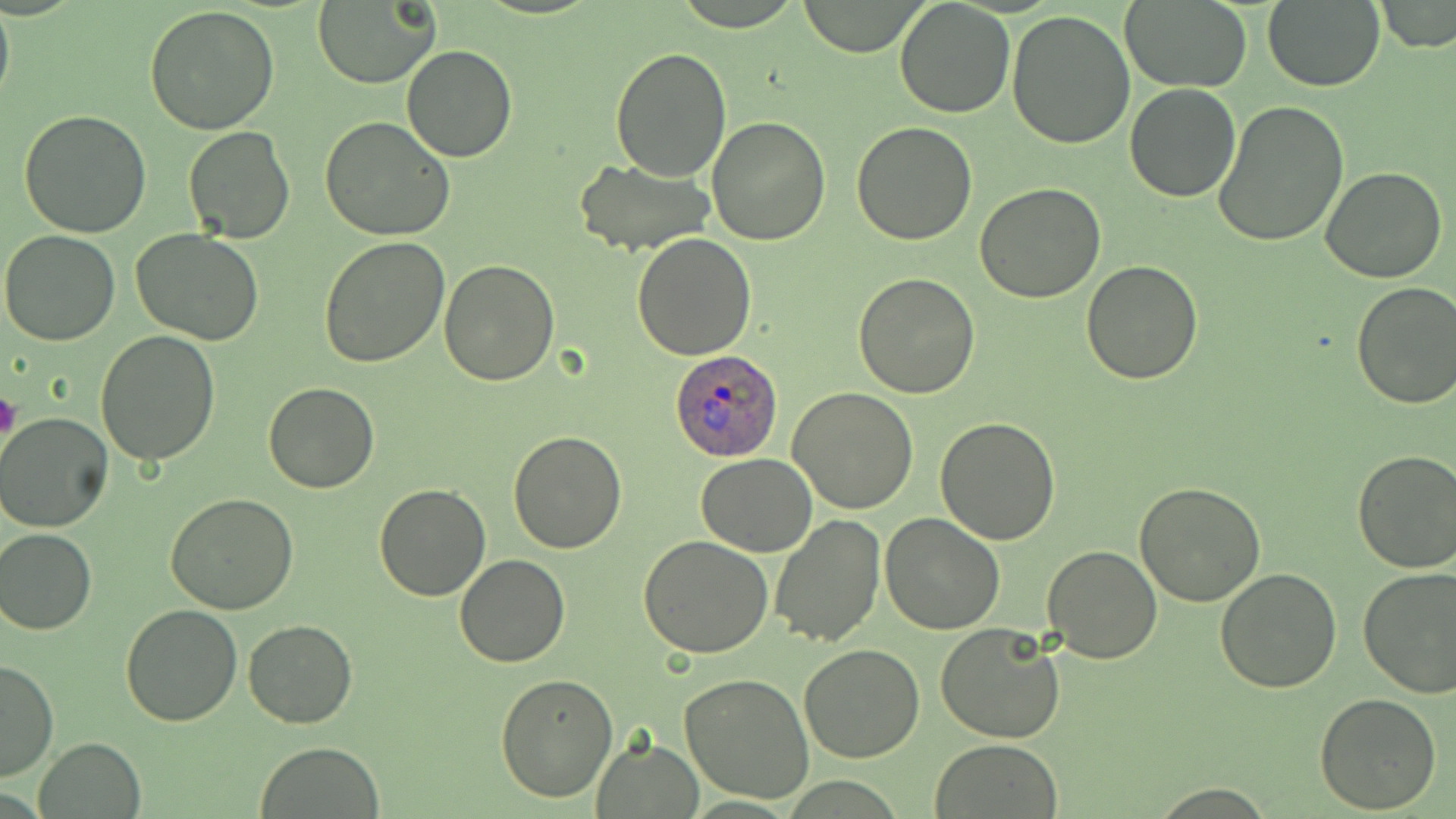
slide-level diagnosis = Plasmodium ovale
stain = May-Grünwald-Giemsa
magnification = 1000x
field of view = single
platelet locations = approximate bounding boxes as (x1, y1, x2, y2) in pixels: (0, 391, 20, 445)
modality = light microscopy
Plasmodium ovale-infected red blood cell locations = approximate bounding boxes as (x1, y1, x2, y2) in pixels: (669, 348, 783, 459)
uninfected red blood cell locations = approximate bounding boxes as (x1, y1, x2, y2) in pixels: (0, 0, 14, 118), (795, 0, 930, 55), (1376, 0, 1456, 52), (313, 1, 438, 88), (894, 1, 1015, 118), (1261, 1, 1384, 92), (1121, 2, 1251, 90), (144, 6, 280, 136), (1005, 8, 1136, 149), (401, 46, 518, 163), (609, 46, 732, 181), (1124, 83, 1242, 201), (1212, 100, 1349, 248), (20, 110, 152, 238), (320, 116, 456, 241), (707, 117, 832, 245), (851, 121, 979, 244), (183, 126, 297, 244), (572, 158, 717, 254), (1319, 166, 1448, 283), (975, 182, 1106, 303), (0, 230, 121, 346), (132, 230, 263, 348), (631, 232, 758, 359), (319, 236, 451, 368), (441, 261, 560, 386), (1081, 261, 1205, 385), (853, 271, 981, 397), (1351, 280, 1456, 410), (96, 329, 220, 466), (263, 382, 379, 494), (787, 386, 920, 515), (1, 412, 116, 531), (934, 416, 1062, 543), (508, 430, 629, 553), (1351, 449, 1456, 574), (697, 455, 819, 557), (1134, 483, 1266, 607), (374, 484, 491, 601), (165, 492, 299, 612), (878, 513, 1005, 634), (770, 514, 885, 648), (2, 526, 96, 634), (640, 536, 773, 658), (1042, 543, 1163, 664), (455, 555, 569, 667), (1214, 568, 1342, 694), (1358, 568, 1456, 699), (120, 603, 243, 726), (243, 618, 357, 729), (935, 622, 1067, 744), (798, 644, 925, 764), (0, 659, 57, 782), (495, 671, 619, 804), (680, 673, 814, 803), (1314, 690, 1442, 812), (35, 737, 145, 818), (931, 738, 1063, 817), (591, 739, 703, 817), (255, 742, 385, 818)
preparation = thin blood smear
image size = 1456×819 pixels